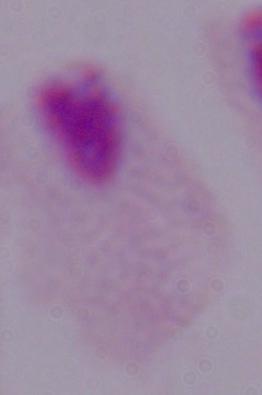
Summary:
  - Identification: trichomonad
  - Modality: micrograph
  - Magnification: 1000x